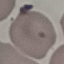
result = negative for malaria parasites
image type = cell patch, automatically extracted from a larger field of view and resized to 64 × 64 pixels
stain = Giemsa
preparation = thin smear
capture = smartphone through the microscope eyepiece